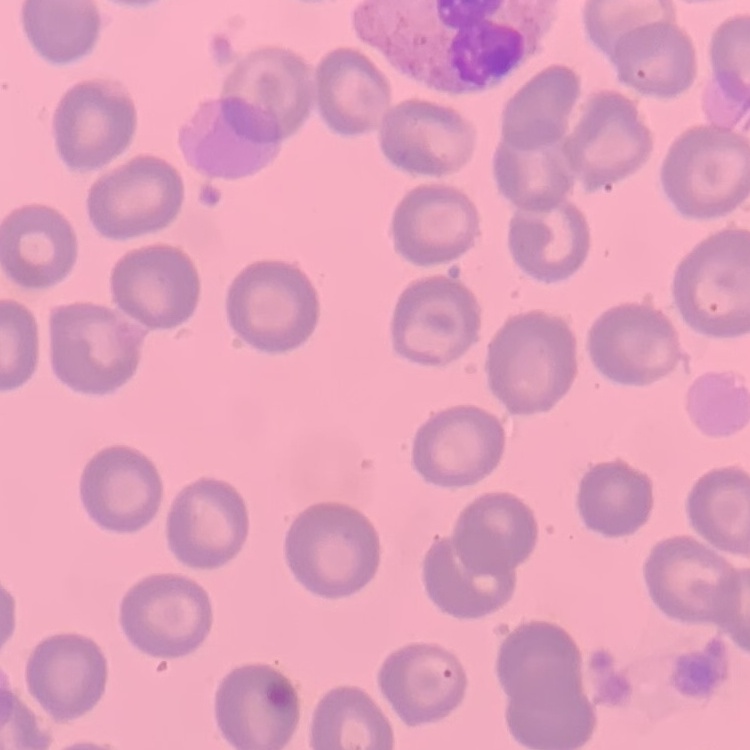

erythrocyte morphology = no rouleaux formation
stain = Field's or Giemsa
image type = square crop of a larger photomicrograph
preparation = thin blood film